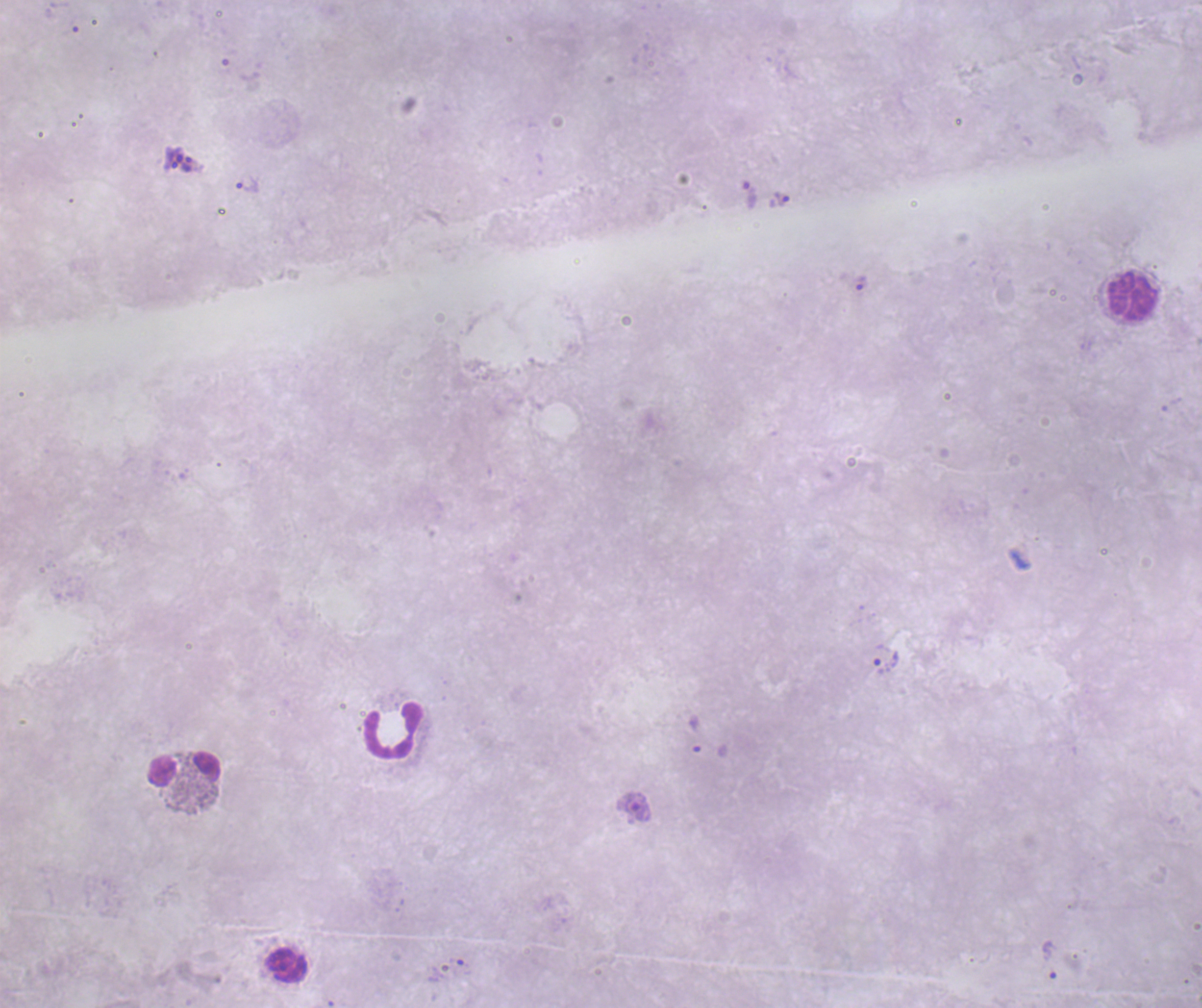

Approximate centers as {x, y} in pixels.
Summary:
  - Schizont locations: {179, 160}
  - Trophozoite locations: {248, 186}, {778, 200}, {860, 282}, {886, 663}, {633, 807}, {1049, 959}
  - Leukocyte locations: {1132, 296}, {393, 730}, {184, 768}, {286, 965}
  - Life-cycle stages observed: trophozoite, schizont
  - Stain: Romanowsky
  - Result: positive for Plasmodium parasites
  - Magnification: 100x
  - Preparation: thick blood film
  - Coloration quality: bad
  - Field of view: single
  - Image size: 1202×1008 pixels
  - Background quality: unsatisfactory
  - Context: previously used in an actual diagnosis